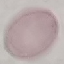

result = no malaria parasites detected
stain = Giemsa
image type = cell patch, automatically extracted from a larger field of view and resized to 64 × 64 pixels
capture = smartphone through the microscope eyepiece
preparation = thin blood smear